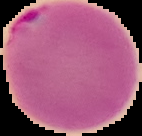

Image is 142×136 pixels. Cell region segmented out of the field of view; the surrounding area is masked to black. From a thin blood smear. Malaria status: parasitized.